Assess the morphology of the erythrocytes.
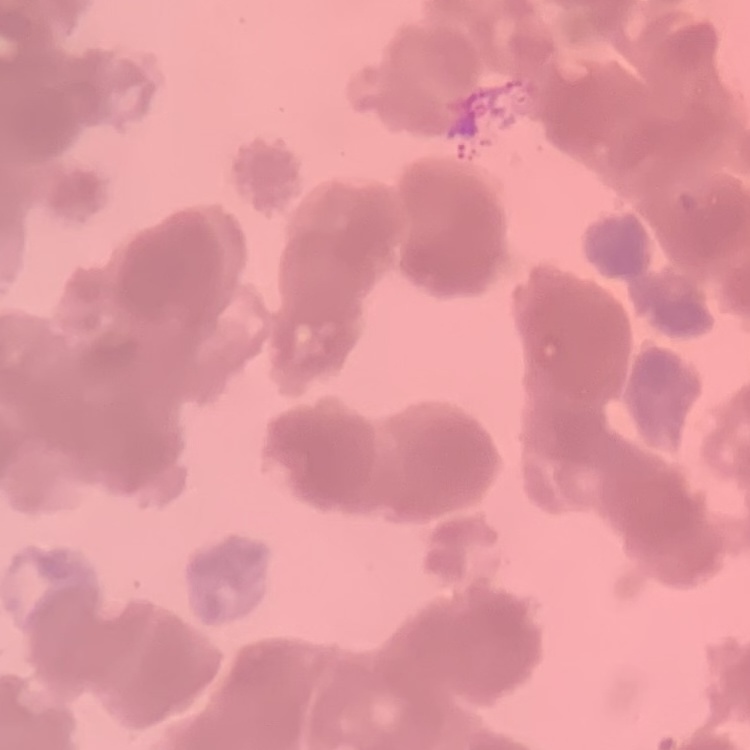
They show rouleaux formation.

stain = Field's or Giemsa
preparation = thin peripheral smear
image type = square crop of a larger photomicrograph